Report the malaria status of this cell.
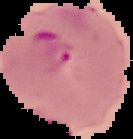

Parasitized.

image type = cell region segmented out of the field of view; surrounding area masked to black
preparation = thin blood film
image size = 133×139 pixels